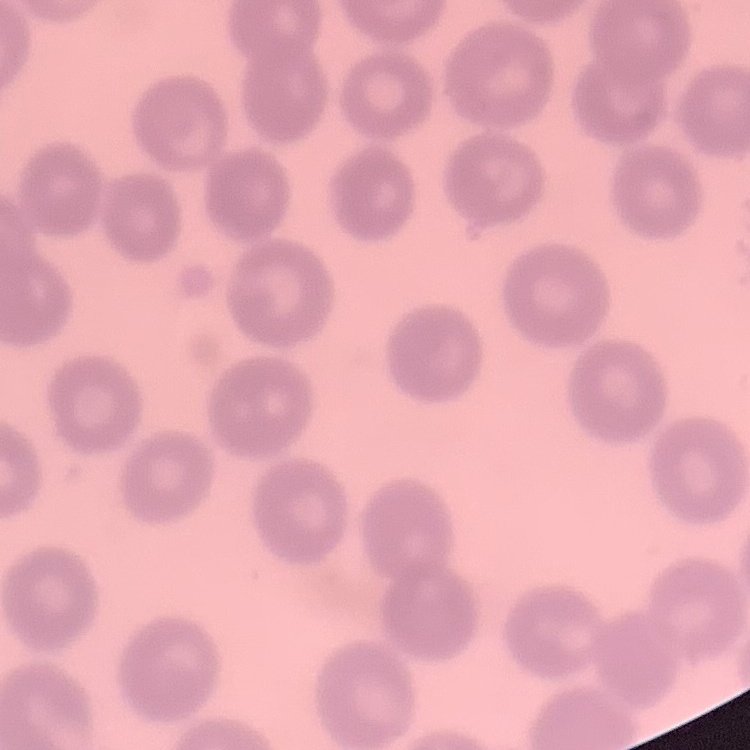
erythrocyte morphology = no rouleaux formation
stain = Field's or Giemsa
preparation = thin blood smear
image type = square crop of a larger photomicrograph